Locate Plasmodium malariae parasites and identify their life-cycle stages.
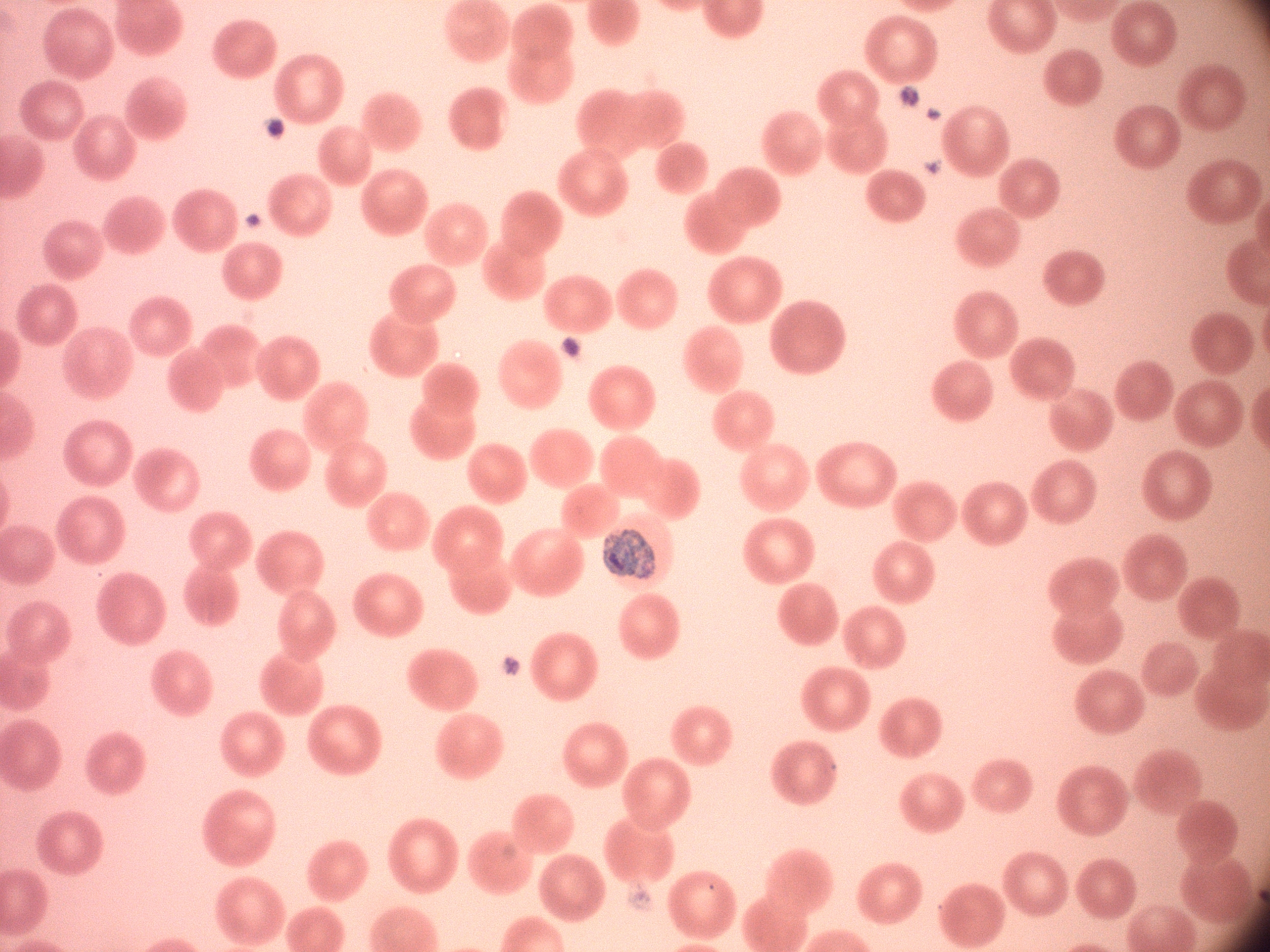

Approximate bounding boxes as [x1, y1, x2, y2] in pixels, from the source annotation, which is not necessarily exhaustive.
Trophozoites: [602, 530, 655, 579].

Acquired with a Leica DM2000 optical microscope and its built-in camera. Image is 1270×952 pixels. Thin blood smear. Captured at 100x magnification. Species: Plasmodium malariae. Single field of view. Giemsa-stained preparation.